Classify this cell by malaria status.
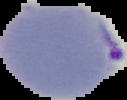

It is parasitized.

Summary:
  - Image size: 127×100 pixels
  - Preparation: thin blood film
  - Image type: segmented cell region on a black background